Locate platelets.
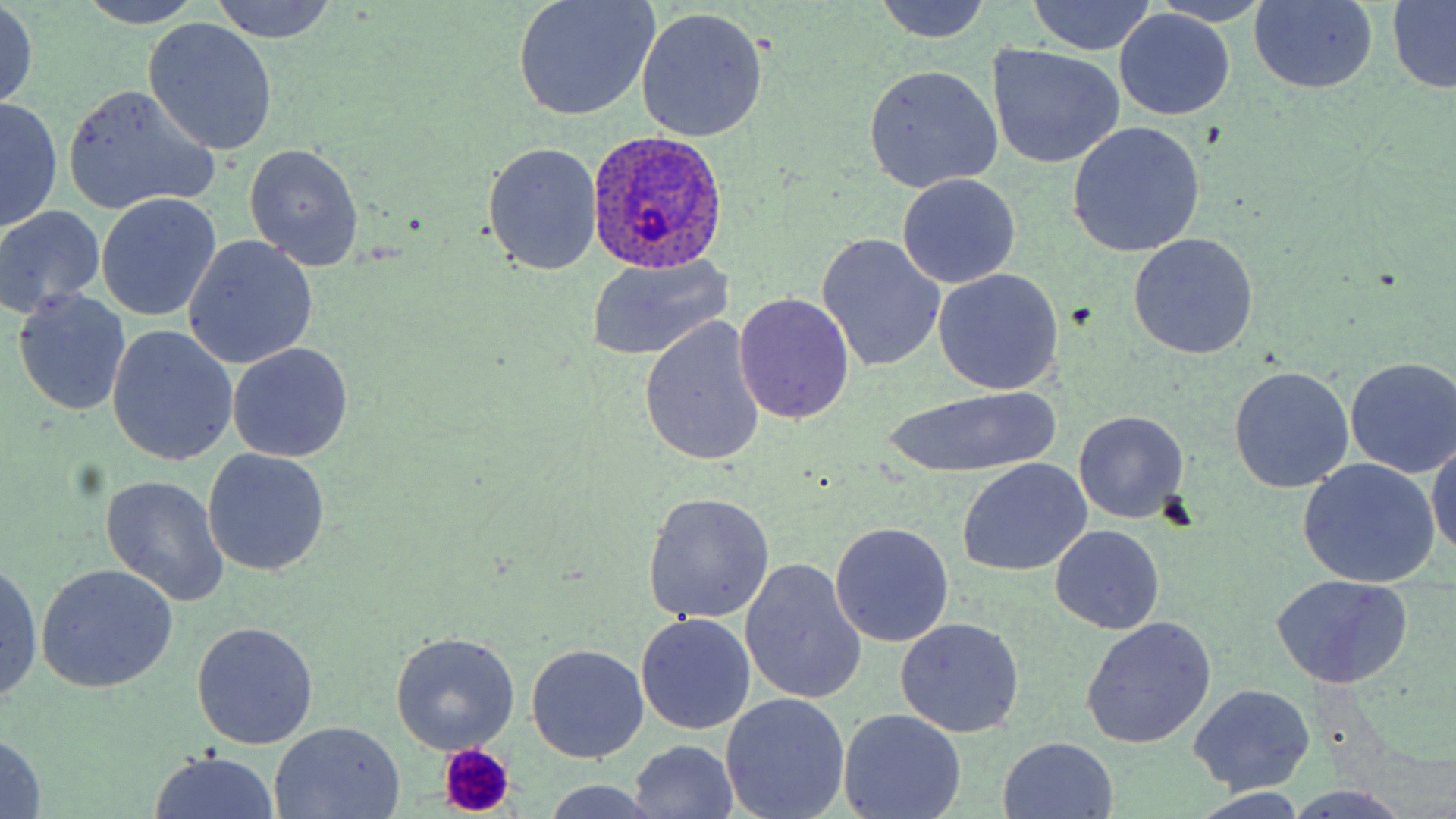
Approximate bounding boxes as [x1, y1, x2, y2] in pixels.
Platelets: [1149, 490, 1198, 530], [438, 744, 517, 815].

Uninfected red blood cell locations: [207, 0, 338, 44], [511, 0, 662, 120], [870, 0, 993, 44], [75, 1, 209, 28], [1028, 1, 1156, 55], [1248, 1, 1377, 93], [1386, 1, 1456, 92], [0, 2, 39, 112], [1148, 2, 1276, 26], [635, 8, 769, 142], [1115, 11, 1234, 121], [143, 19, 278, 155], [987, 44, 1126, 170], [864, 65, 1004, 192], [60, 88, 218, 216], [1, 96, 61, 234], [1066, 123, 1205, 256], [484, 142, 600, 276], [244, 143, 364, 270], [897, 175, 1021, 289], [96, 192, 222, 321], [0, 205, 106, 320], [1128, 233, 1259, 360], [817, 235, 946, 372], [183, 237, 317, 368], [585, 256, 734, 361], [931, 269, 1064, 396], [14, 287, 132, 416], [733, 294, 854, 425], [638, 317, 766, 468], [107, 326, 237, 466], [227, 342, 353, 463], [1346, 357, 1456, 477], [1229, 367, 1354, 492], [884, 385, 1059, 478], [1074, 411, 1188, 524], [1428, 436, 1456, 562], [202, 449, 329, 577], [1298, 458, 1440, 587], [957, 461, 1089, 575], [100, 473, 229, 608], [644, 492, 774, 624], [831, 523, 952, 645], [1050, 525, 1165, 635], [0, 560, 43, 705], [741, 561, 867, 705], [39, 562, 178, 691], [1271, 577, 1412, 688], [636, 613, 756, 735], [895, 616, 1025, 738], [1083, 617, 1216, 749], [192, 622, 318, 749], [391, 632, 519, 754], [526, 644, 649, 763], [1189, 685, 1315, 794], [723, 695, 850, 819], [839, 707, 967, 819], [269, 721, 407, 817], [1, 732, 49, 817], [998, 736, 1119, 818], [627, 739, 740, 817], [147, 751, 286, 819], [540, 778, 662, 818], [1282, 787, 1422, 819]. Plasmodium ovale-infected red blood cell locations: [587, 130, 729, 273]. Slide-level diagnosis: Plasmodium ovale. Single field of view. May-Grünwald-Giemsa-stained preparation. Image is 1456×819 pixels. Captured at 1000x magnification. Thin blood smear. Light microscopy.